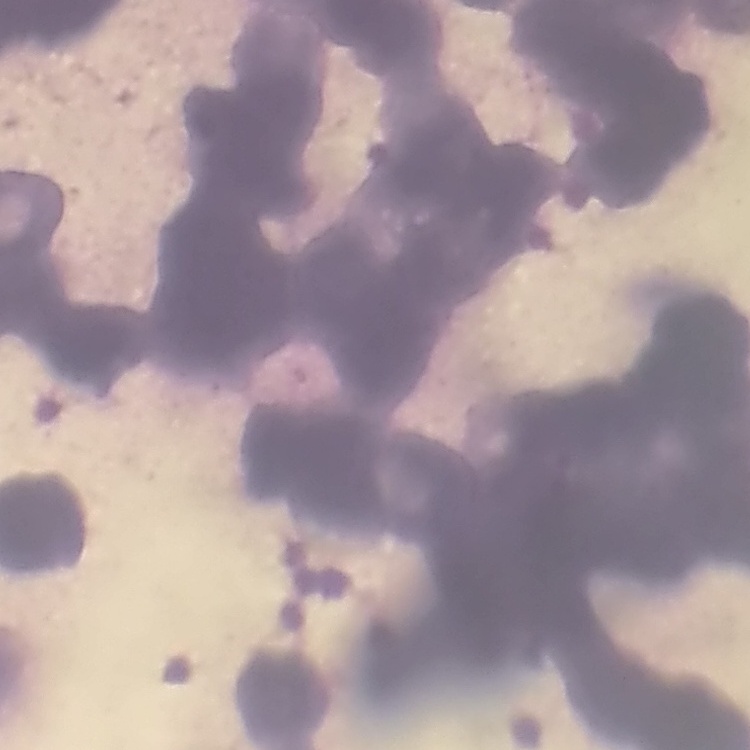

The erythrocytes show rouleaux formation. One tile cut from a larger photomicrograph. Field's or Giemsa stain. Thin peripheral smear.